Outline each blood parasite and name the species.
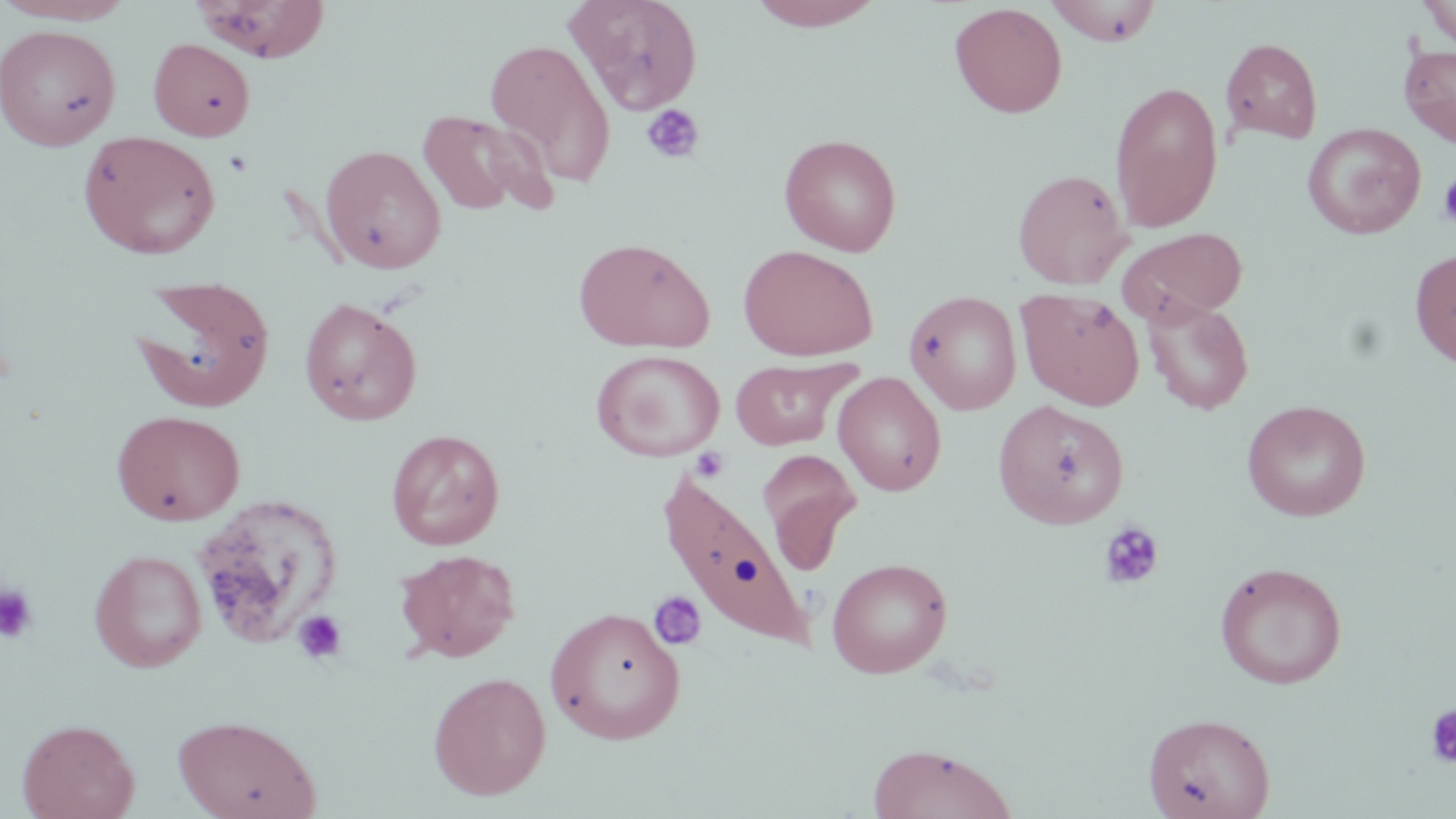
No blood parasites seen.

Summary:
  - Coordinate format: approximate bounding boxes as (x1, y1, x2, y2) in pixels
  - Uninfected red blood cell locations: (0, 0, 137, 25), (193, 0, 331, 63), (565, 0, 704, 115), (747, 0, 886, 31), (1418, 0, 1456, 47), (1046, 1, 1162, 46), (949, 2, 1067, 118), (0, 23, 121, 151), (148, 38, 256, 141), (483, 38, 617, 188), (1221, 38, 1323, 143), (1399, 43, 1456, 147), (1109, 81, 1223, 234), (415, 108, 550, 218), (1303, 123, 1426, 239), (77, 130, 221, 259), (779, 133, 902, 256), (320, 144, 446, 274), (1012, 168, 1132, 289), (1117, 226, 1248, 326), (572, 237, 715, 354), (738, 244, 879, 361), (1410, 250, 1456, 367), (130, 274, 276, 413), (1017, 288, 1145, 410), (905, 290, 1022, 415), (298, 296, 422, 425), (1142, 297, 1255, 415), (591, 348, 725, 462), (731, 357, 855, 450), (833, 372, 946, 496), (992, 399, 1129, 529), (1242, 400, 1371, 521), (112, 409, 246, 525), (386, 428, 505, 550), (757, 448, 861, 565), (657, 465, 822, 652), (191, 495, 345, 650), (394, 548, 521, 662), (89, 549, 207, 673), (826, 557, 952, 678), (1214, 562, 1347, 689), (545, 606, 686, 744), (428, 670, 551, 800), (1143, 712, 1275, 819), (173, 714, 321, 819), (17, 717, 140, 819), (867, 743, 1017, 819)
  - Platelet locations: (641, 104, 705, 164), (222, 149, 254, 177), (1438, 174, 1456, 230), (1099, 520, 1164, 590), (0, 583, 39, 644), (647, 590, 706, 652), (293, 609, 348, 665), (1424, 703, 1456, 768)
  - Slide-level diagnosis: negative for blood parasites
  - Magnification: 1000x
  - Image size: 1456×819 pixels
  - Modality: light microscopy
  - Preparation: thin blood film
  - Stain: May-Grünwald-Giemsa
  - Field of view: single